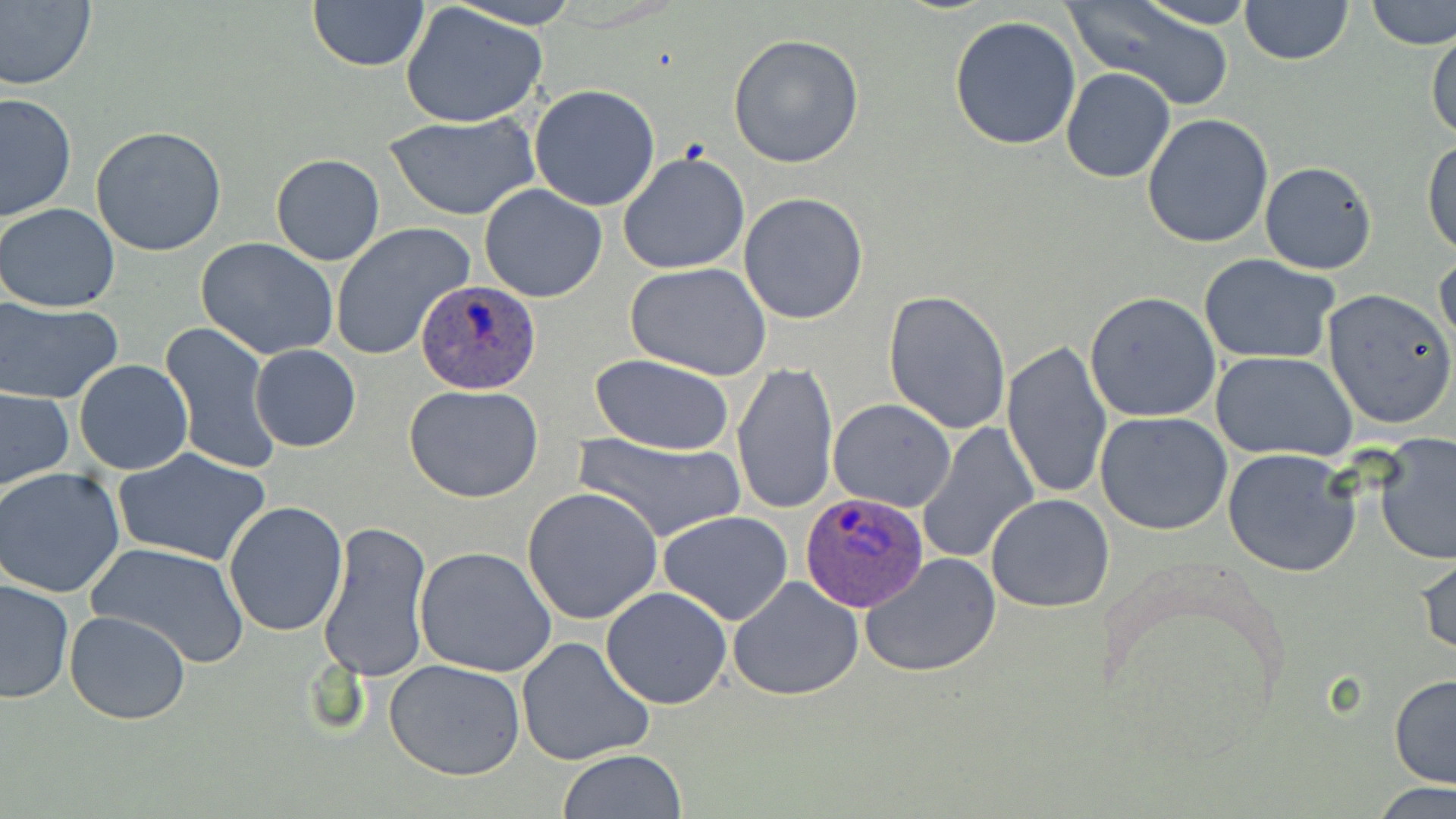
Summary:
  - Coordinate format: approximate bounding boxes as (x1,y1)-(x2,y2) corner pairs in pixels
  - Uninfected red blood cell locations: (0,0)-(96,90), (307,0)-(428,71), (441,0)-(585,29), (1069,0)-(1234,109), (1240,0)-(1354,65), (1364,0)-(1456,51), (1134,1)-(1260,29), (399,3)-(549,128), (949,16)-(1082,150), (1427,24)-(1456,143), (729,33)-(864,170), (1061,68)-(1176,184), (528,85)-(660,211), (0,91)-(76,222), (386,110)-(539,221), (1141,113)-(1276,250), (89,126)-(228,256), (1424,140)-(1456,258), (618,152)-(750,276), (271,153)-(385,267), (1259,161)-(1378,275), (478,184)-(607,303), (738,192)-(869,325), (0,202)-(120,314), (331,223)-(475,362), (195,237)-(338,359), (1434,250)-(1456,353), (1198,253)-(1342,365), (625,262)-(774,384), (1321,289)-(1455,430), (883,290)-(1012,435), (1083,292)-(1223,424), (0,298)-(126,404), (158,322)-(280,477), (1002,338)-(1115,501), (250,344)-(361,452), (1211,351)-(1359,460), (590,355)-(739,454), (74,359)-(193,475), (732,361)-(839,516), (404,383)-(544,503), (0,387)-(74,490), (828,399)-(957,512), (1096,412)-(1232,536), (914,421)-(1041,565), (570,432)-(748,545), (1376,432)-(1456,565), (1222,449)-(1361,578), (115,450)-(271,566), (0,467)-(128,597), (521,485)-(665,624), (986,492)-(1114,611), (223,500)-(348,636), (658,512)-(794,626), (318,520)-(434,683), (85,541)-(250,667), (413,547)-(557,679), (1416,547)-(1456,660), (860,553)-(1004,676), (727,577)-(863,701), (0,579)-(74,704), (601,587)-(732,710), (64,609)-(192,725), (516,634)-(656,767), (385,659)-(526,781), (1389,673)-(1456,790), (557,749)-(688,818), (1371,781)-(1454,818)
  - Plasmodium ovale-infected red blood cell locations: (414,277)-(542,395), (800,489)-(927,610)
  - Slide-level diagnosis: Plasmodium ovale
  - Magnification: 1000x
  - Preparation: thin blood film
  - Image size: 1456×819 pixels
  - Stain: May-Grünwald-Giemsa
  - Field of view: single
  - Modality: optical microscopy